Locate and identify every blood parasite.
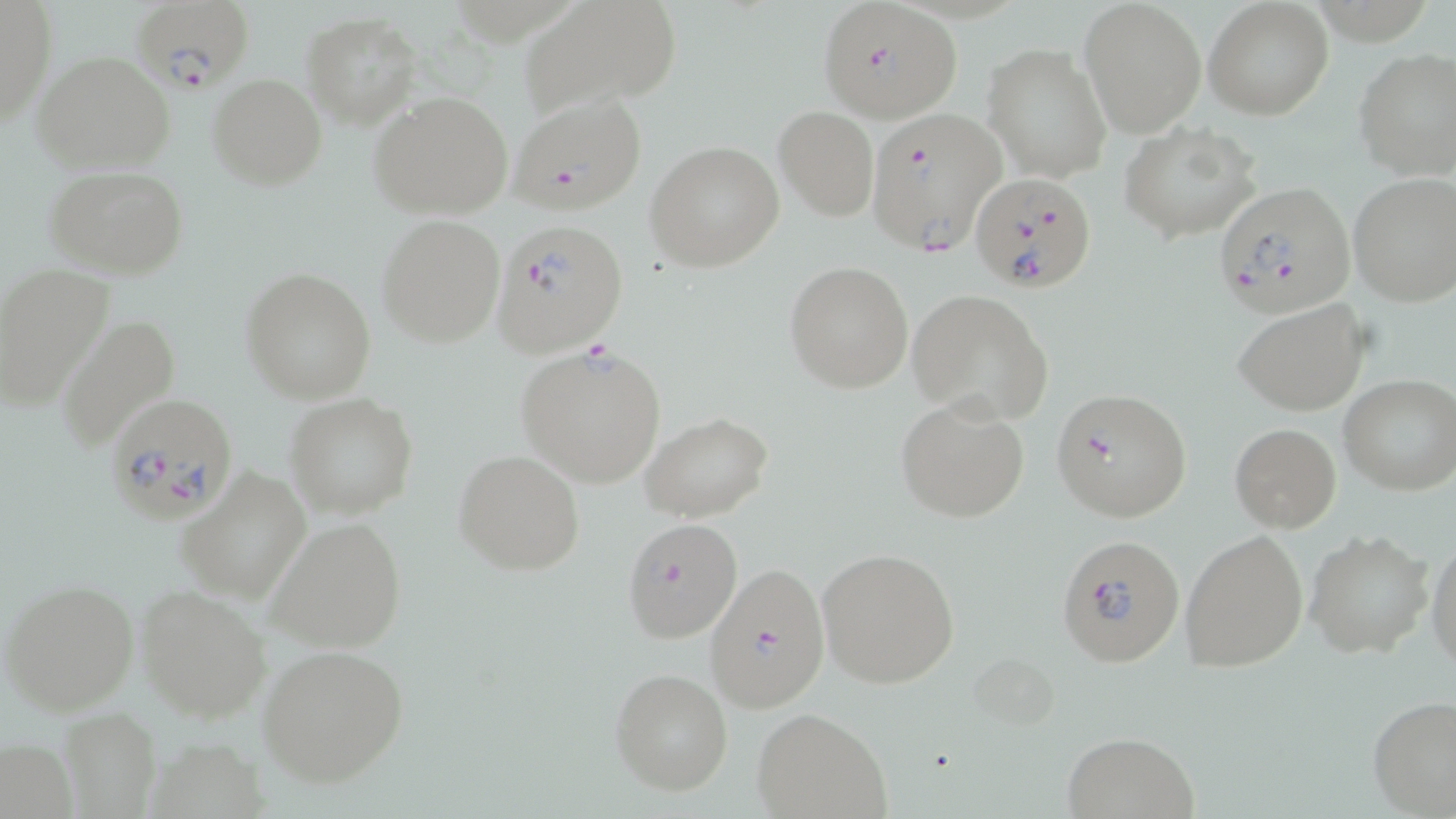
Approximate bounding boxes as named x1/y1/x2/y2 corners in pixels.
Plasmodium falciparum-infected red blood cells: (x1=128, y1=0, x2=256, y2=96), (x1=819, y1=6, x2=962, y2=124), (x1=506, y1=94, x2=649, y2=215), (x1=866, y1=108, x2=1006, y2=258), (x1=971, y1=173, x2=1097, y2=293), (x1=1217, y1=182, x2=1356, y2=316), (x1=491, y1=218, x2=628, y2=356), (x1=1050, y1=387, x2=1193, y2=522), (x1=103, y1=391, x2=241, y2=525), (x1=620, y1=518, x2=743, y2=644), (x1=1056, y1=533, x2=1186, y2=667), (x1=704, y1=563, x2=830, y2=712).
No Plasmodium ovale, Plasmodium malariae, Plasmodium vivax, Babesia divergens, or Trypanosoma brucei observed.

slide-level diagnosis = Plasmodium falciparum
field of view = one of a larger specimen
stain = May-Grünwald-Giemsa
modality = light microscopy
image size = 1456×819 pixels
magnification = 1000x
preparation = thin blood film
uninfected red blood cell locations = approximate bounding boxes as named x1/y1/x2/y2 corners in pixels: (x1=1, y1=1, x2=56, y2=128), (x1=517, y1=1, x2=684, y2=116), (x1=1203, y1=1, x2=1332, y2=120), (x1=1080, y1=2, x2=1205, y2=134), (x1=301, y1=13, x2=421, y2=127), (x1=983, y1=42, x2=1112, y2=184), (x1=1355, y1=47, x2=1456, y2=179), (x1=30, y1=52, x2=177, y2=174), (x1=208, y1=74, x2=326, y2=190), (x1=369, y1=92, x2=514, y2=219), (x1=774, y1=106, x2=878, y2=220), (x1=1119, y1=121, x2=1264, y2=241), (x1=646, y1=141, x2=783, y2=271), (x1=44, y1=164, x2=191, y2=280), (x1=1347, y1=172, x2=1456, y2=307), (x1=376, y1=216, x2=506, y2=347), (x1=784, y1=260, x2=913, y2=392), (x1=0, y1=263, x2=114, y2=408), (x1=240, y1=268, x2=376, y2=404), (x1=908, y1=290, x2=1056, y2=426), (x1=1231, y1=297, x2=1372, y2=418), (x1=56, y1=315, x2=181, y2=452), (x1=516, y1=344, x2=667, y2=488), (x1=1338, y1=376, x2=1455, y2=495), (x1=285, y1=394, x2=417, y2=518), (x1=895, y1=394, x2=1031, y2=523), (x1=640, y1=414, x2=773, y2=524), (x1=1229, y1=423, x2=1340, y2=532), (x1=452, y1=450, x2=585, y2=575), (x1=177, y1=466, x2=312, y2=604), (x1=264, y1=515, x2=409, y2=655), (x1=1179, y1=529, x2=1309, y2=674), (x1=1305, y1=530, x2=1434, y2=658), (x1=1427, y1=533, x2=1456, y2=673), (x1=818, y1=547, x2=961, y2=689), (x1=2, y1=577, x2=140, y2=716), (x1=137, y1=584, x2=271, y2=723), (x1=256, y1=643, x2=411, y2=787), (x1=610, y1=668, x2=733, y2=795), (x1=1367, y1=695, x2=1456, y2=819), (x1=59, y1=707, x2=161, y2=818), (x1=753, y1=708, x2=893, y2=818), (x1=1062, y1=731, x2=1200, y2=818)